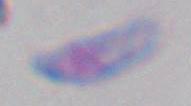
Summary:
  - Magnification: 1000x
  - Identification: Toxoplasma gondii
  - Modality: micrograph